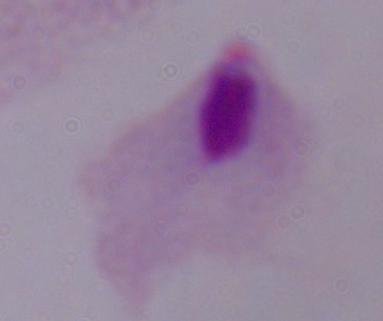

identification: trichomonad
magnification: 1000x
modality: micrograph